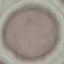

Summary:
  - Result: negative for malaria parasites
  - Capture: smartphone through the microscope eyepiece
  - Image type: automatically extracted cell patch, resized to 64 × 64 pixels
  - Stain: Giemsa
  - Preparation: thin blood smear